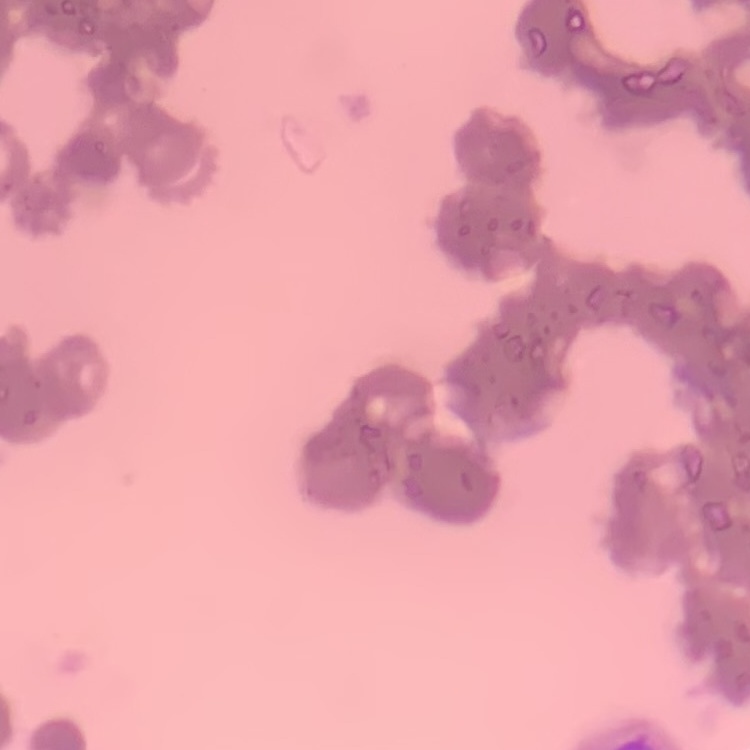 The red blood cells show rouleaux formation. Thin blood film. Stained with either Field's or Giemsa. One tile cut from a larger photomicrograph.